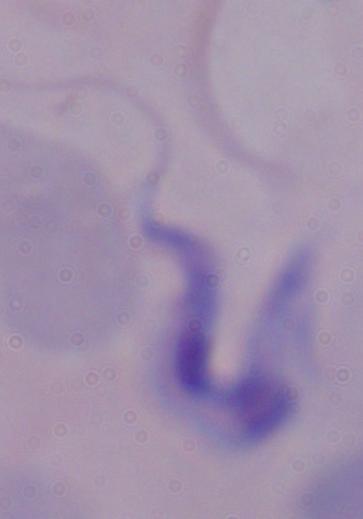

modality = photomicrograph
identification = trypanosome
magnification = 1000x